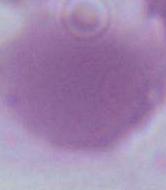

1000x magnification. Photomicrograph. A red blood cell is shown.